Give a bounding box for every parasitised red blood cell, every trophozoite, every gametocyte, every leukocyte, and every artifact (platelet-like body, stain precipitate, or debris).
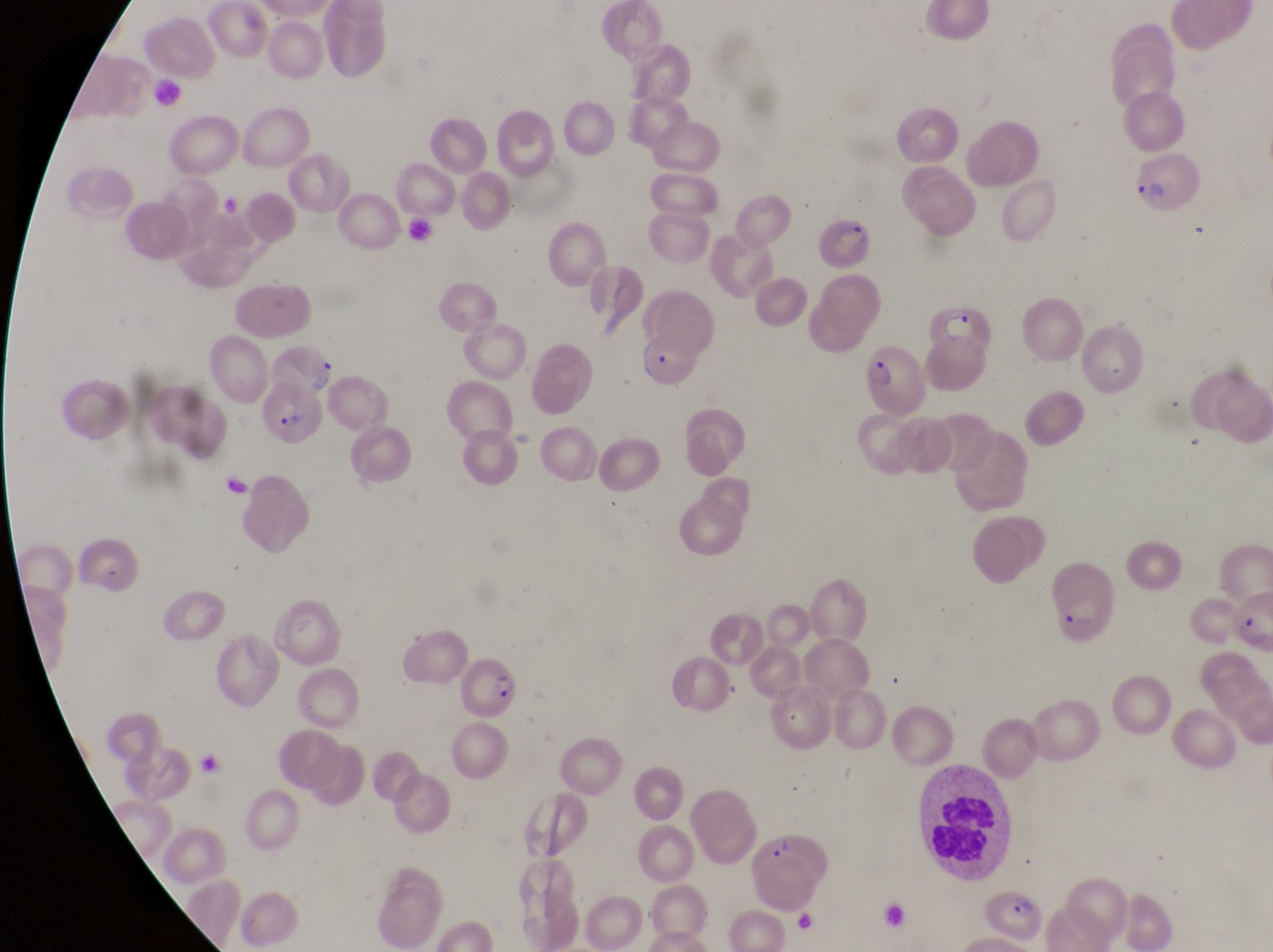
Approximate bounding boxes as left top right bottom in pixels.
Parasitised red blood cells: 1130 155 1210 218; 817 215 887 278; 917 295 997 387; 863 347 930 417; 262 380 331 448; 77 534 135 596; 1055 554 1117 641; 460 661 522 724; 761 829 831 912; 983 881 1043 949.
Leukocytes: 150 76 191 117; 919 768 1017 877.

Image is 1273×952 pixels. Thin blood film. Magnification of 1000x. Sample from Uganda. Single field of view. Photographed through the eyepiece of an Olympus CX-23 microscope with a smartphone camera.